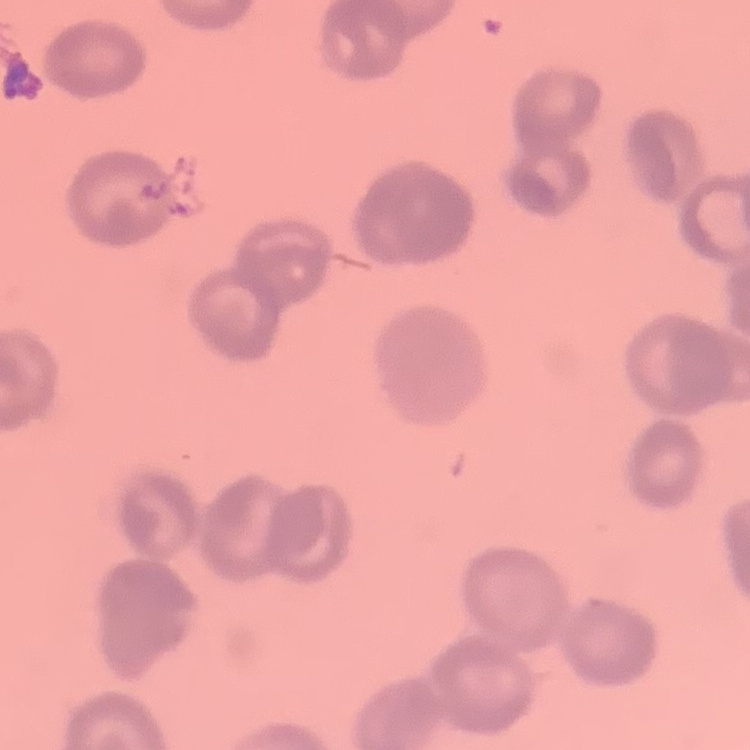
{
  "erythrocyte_morphology": "rouleaux formation",
  "stain": "Field's or Giemsa",
  "preparation": "thin peripheral smear",
  "image_type": "one tile cut from a larger photomicrograph"
}